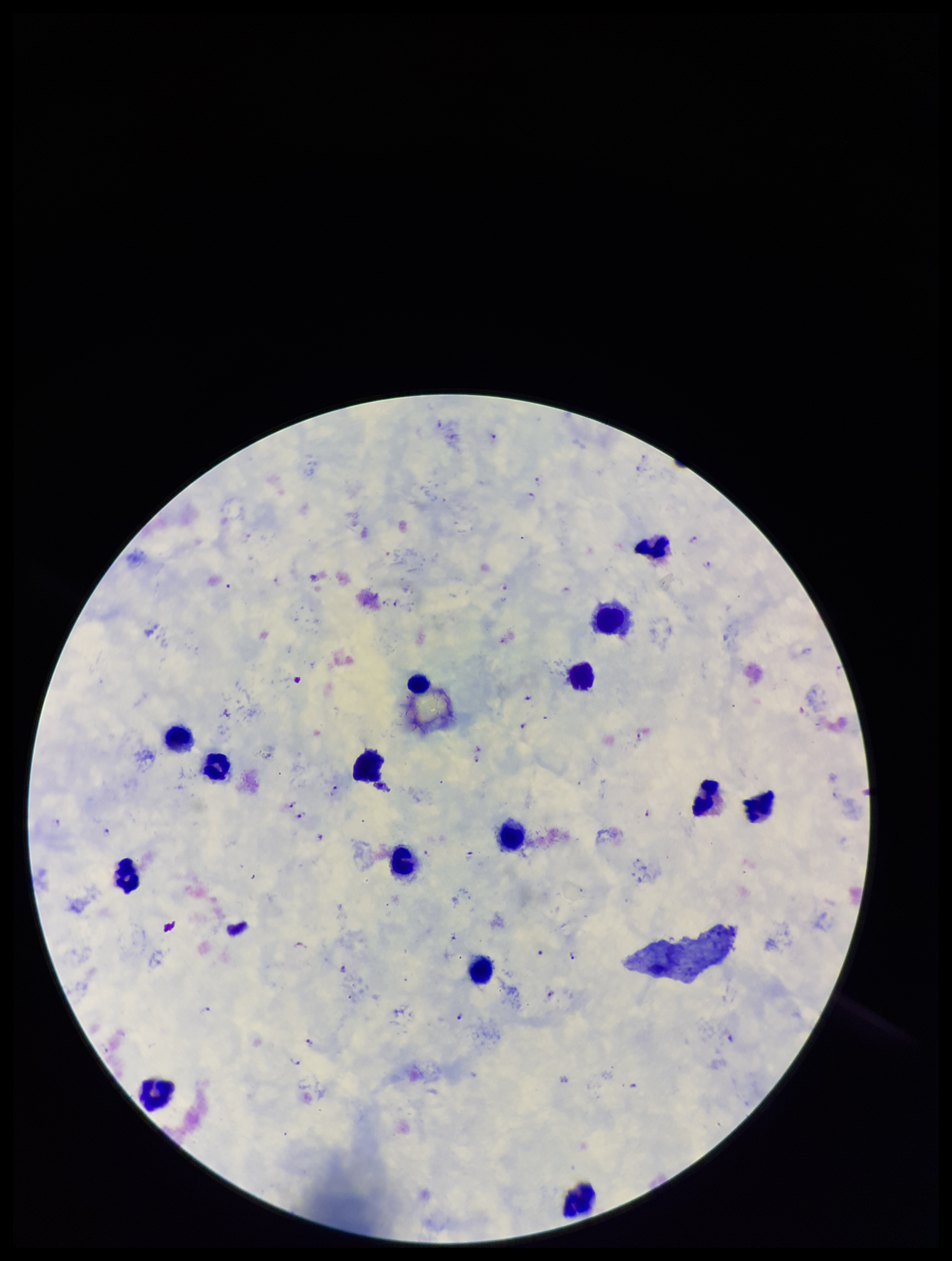
Summary:
  - Image size: 952×1261 pixels
  - Plasmodium parasites: detected
  - Capture: smartphone photograph through the microscope eyepiece
  - Field of view: one from this slide
  - Species reported for this patient: Plasmodium falciparum
  - Stain: Giemsa
  - Parasite count: 26
  - Leukocyte count: 15
  - Patient malaria status: positive
  - Preparation: thick